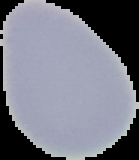

Image is 139×160 pixels. The area outside the segmented cell region is set to black. From a thin blood smear. Result: no Plasmodium parasites detected.